Classify this cell by malaria status.
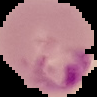
Parasitized.

image type = segmented cell region with the area outside set to black
preparation = thin blood film
image size = 97×97 pixels